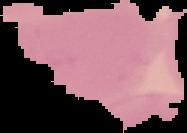

Summary:
  - Preparation: thin blood film
  - Image size: 187×133 pixels
  - Image type: segmented cell region on a black background
  - Malaria status: uninfected